Comment on the morphology of the erythrocytes.
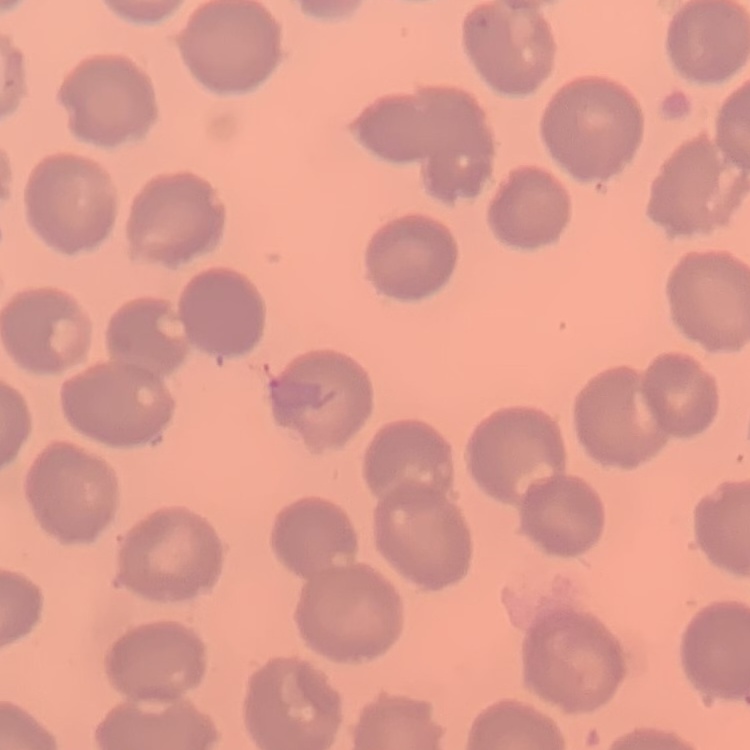

They show no rouleaux formation.

Field's or Giemsa stain. Thin peripheral smear. One tile cut from a larger photomicrograph.